Classify this cell by malaria status.
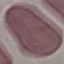
Uninfected.

Cell patch, automatically extracted from a larger field of view and resized to 64 × 64 pixels. Thin blood smear. Acquired by smartphone through the microscope eyepiece. Giemsa-stained preparation.